Locate every malaria parasite.
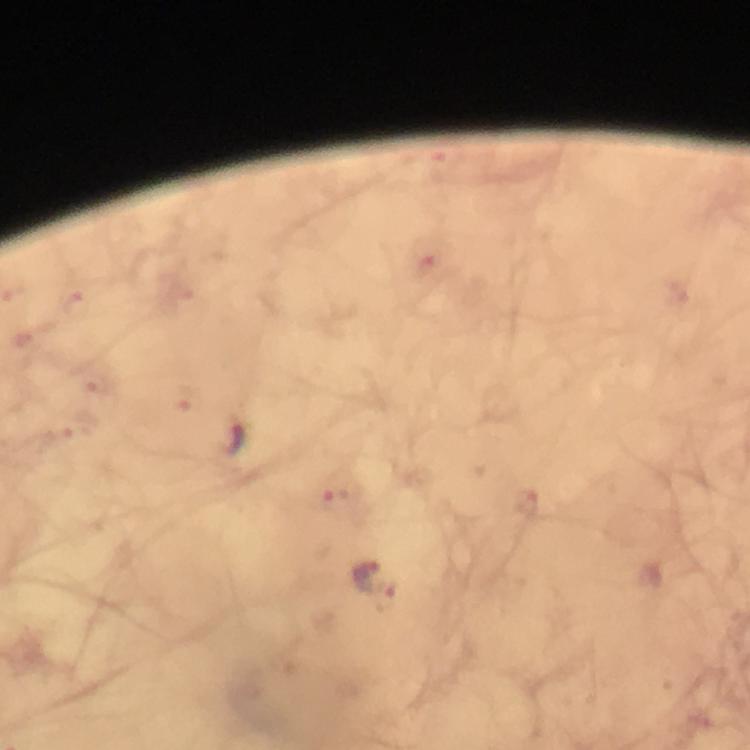

Approximate centers as {x, y} in pixels.
Malaria parasites: {424, 251}, {75, 303}, {94, 378}, {185, 398}, {75, 425}, {237, 440}, {339, 501}, {526, 505}, {364, 572}, {381, 596}.

Image is 750×750 pixels. Giemsa stain. Thick smear. Cropped region of a single field of view. 100x magnification. Immersion oil applied. Photographed with a smartphone mounted on the microscope. From a diagnostic examination for malaria.